Assess the morphology of the red blood cells.
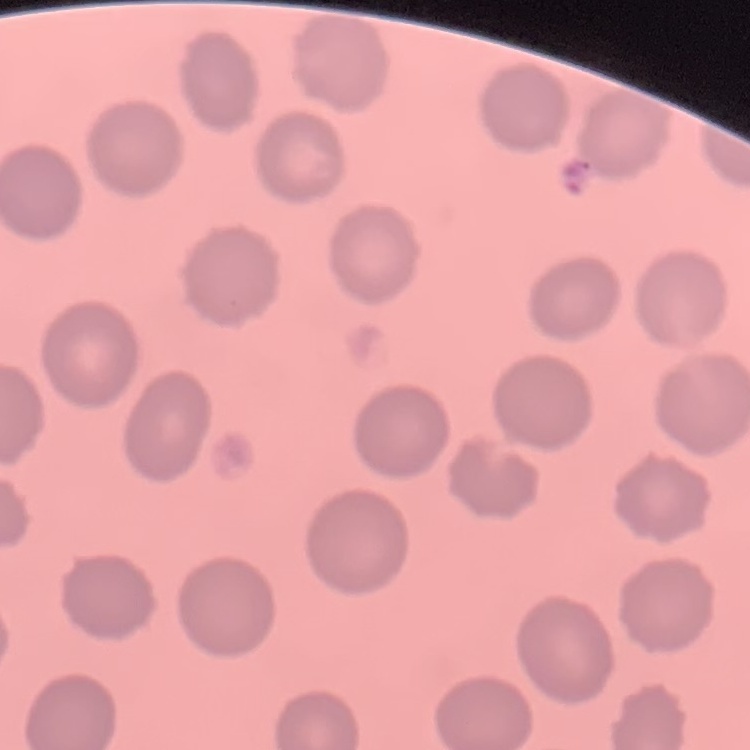
They show no rouleaux formation.

stain: Field's or Giemsa
image_type: one tile cut from a larger photomicrograph
preparation: thin peripheral smear